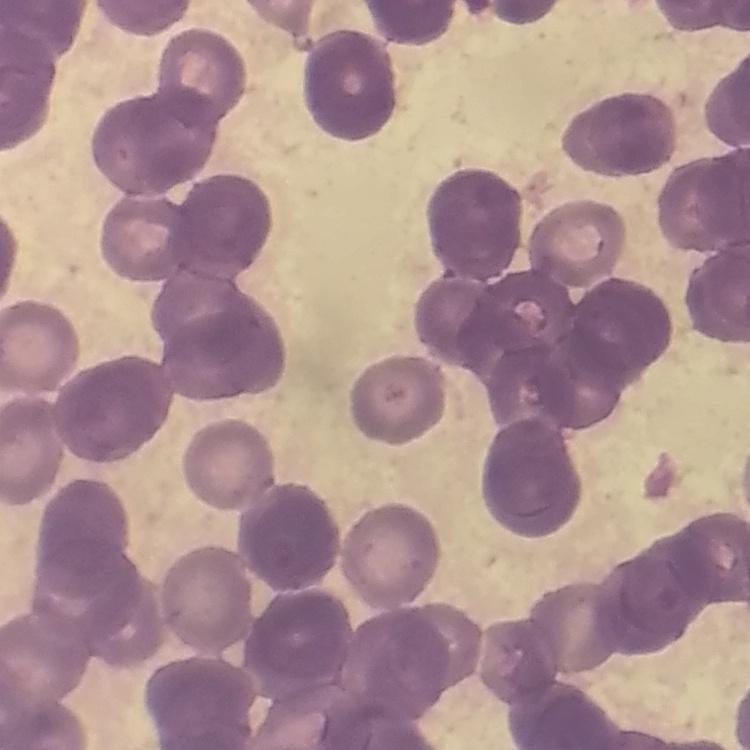
erythrocyte morphology = rouleaux formation
stain = Field's or Giemsa
image type = square crop of a larger photomicrograph
preparation = thin blood smear